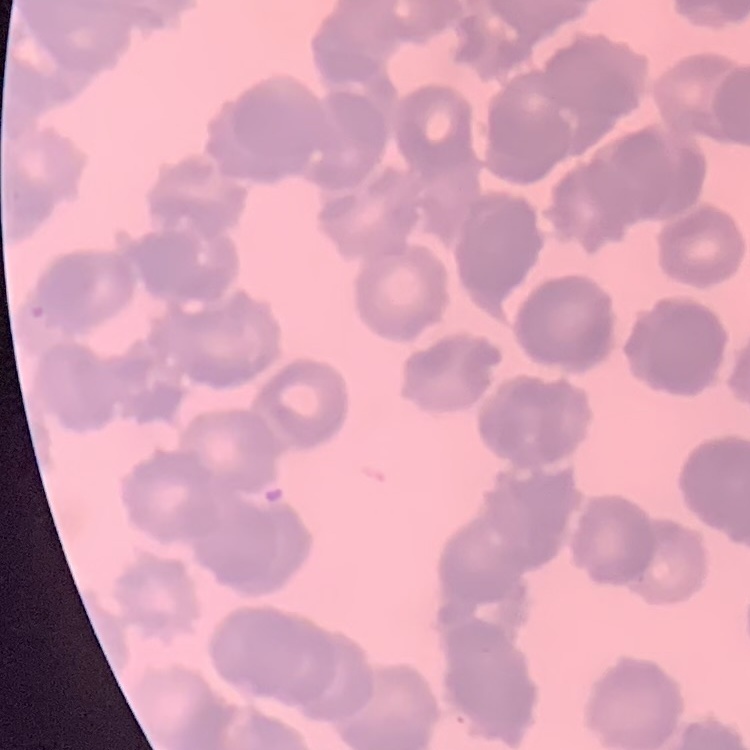

red_blood_cell_morphology: rouleaux formation
image_type: square crop of a larger photomicrograph
stain: Field's or Giemsa
preparation: thin blood smear